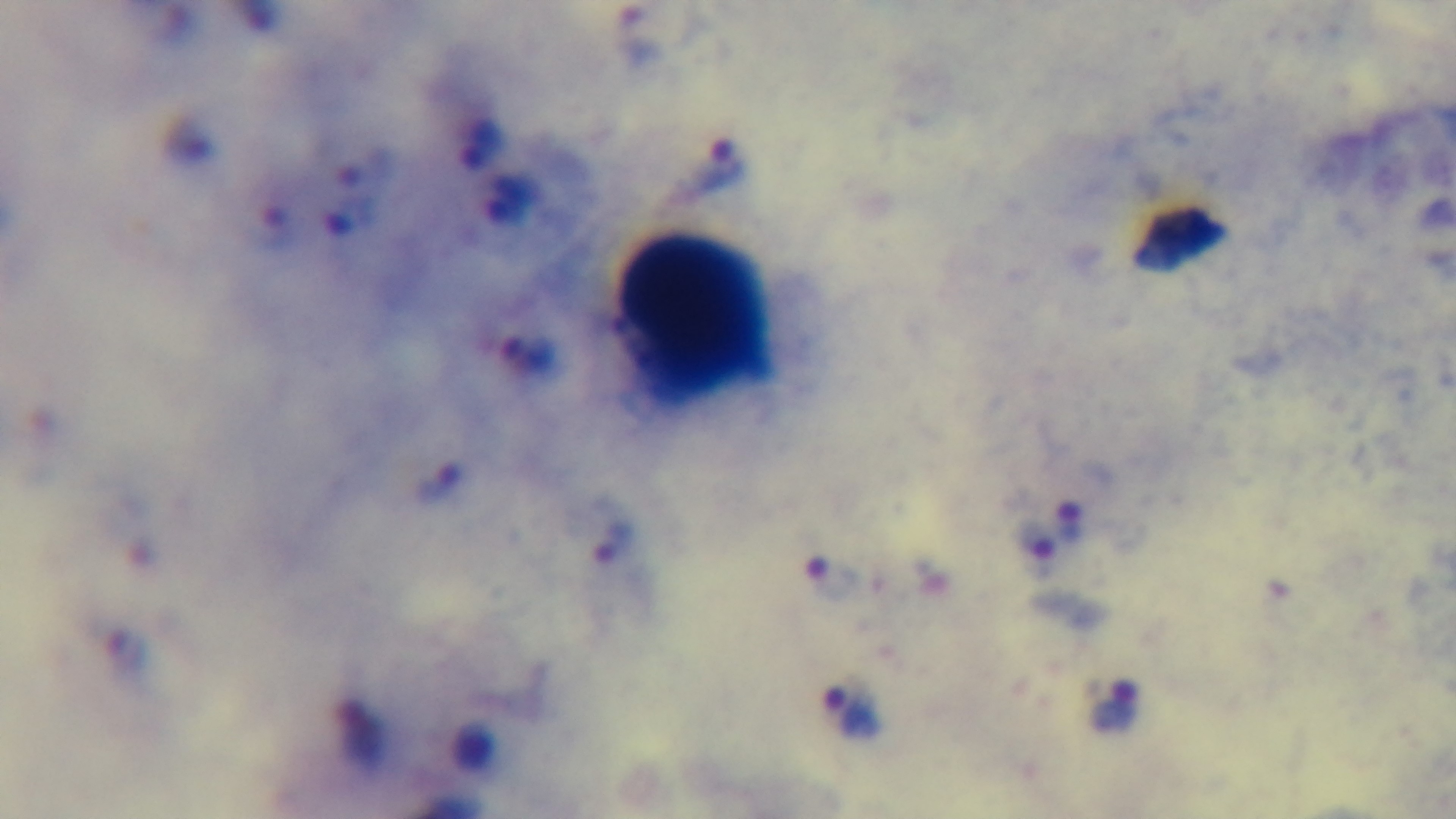
One field from the slide. Malaria status: positive. Mounted 4K digital camera. Preparation: thick. 100x oil-immersion objective. Photomicrograph. Giemsa-stained.